Classify this cell by malaria status.
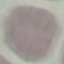
Uninfected.

Summary:
  - Stain: Giemsa
  - Image type: cell patch, automatically extracted from a larger field of view and resized to 64 × 64 pixels
  - Preparation: thin blood smear
  - Capture: smartphone camera at the microscope eyepiece